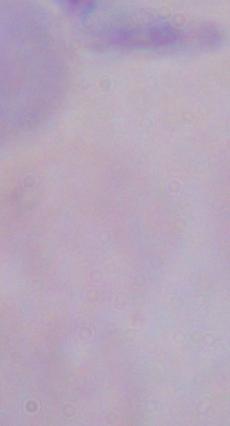
Summary:
  - Magnification: 1000x
  - Identification: trypanosome
  - Modality: photomicrograph